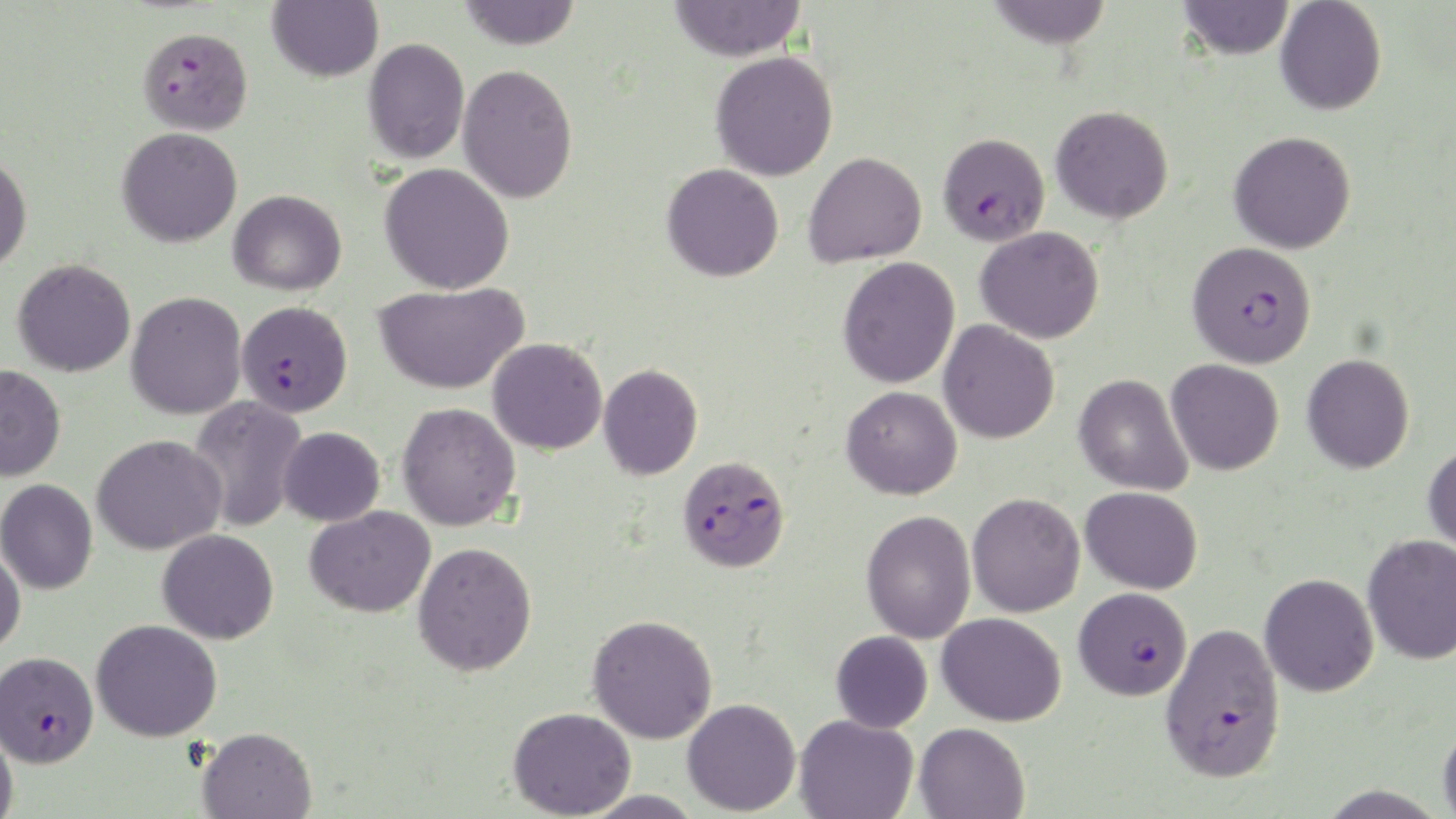
Summary:
  - Coordinate format: approximate bounding boxes as (x1,y1)-(x2,y2) corner pairs in pixels
  - Plasmodium falciparum-infected red blood cell locations: (137,26)-(253,135), (938,132)-(1050,246), (1187,241)-(1317,368), (236,301)-(353,416), (676,454)-(791,572), (1074,587)-(1192,700), (1160,623)-(1286,783), (0,650)-(98,767)
  - Uninfected red blood cell locations: (267,0)-(383,82), (456,0)-(581,50), (668,0)-(806,62), (986,0)-(1113,49), (1177,0)-(1294,60), (1275,0)-(1387,115), (363,37)-(470,164), (710,51)-(838,181), (457,64)-(578,204), (1051,105)-(1173,223), (116,126)-(243,248), (1228,131)-(1356,254), (0,152)-(32,273), (803,152)-(927,268), (380,163)-(515,294), (661,163)-(784,282), (228,189)-(346,295), (975,226)-(1104,344), (837,256)-(960,388), (12,258)-(136,377), (373,281)-(529,395), (126,291)-(247,420), (938,320)-(1060,444), (487,338)-(608,455), (1302,353)-(1414,474), (1166,359)-(1284,476), (599,363)-(703,480), (0,364)-(66,481), (1074,373)-(1193,496), (841,386)-(962,500), (188,396)-(308,532), (397,402)-(522,531), (279,426)-(385,526), (91,434)-(227,555), (1423,444)-(1456,556), (0,479)-(98,594), (1081,486)-(1203,594), (967,492)-(1086,617), (305,506)-(436,618), (861,510)-(976,643), (157,528)-(279,644), (1362,533)-(1456,664), (413,541)-(537,676), (0,545)-(26,655), (1259,573)-(1379,697), (937,612)-(1067,726), (587,614)-(718,744), (91,618)-(222,742), (831,630)-(933,733), (682,698)-(801,816), (508,706)-(636,818), (794,714)-(918,819), (914,722)-(1030,819), (1438,722)-(1456,819), (0,725)-(19,818), (197,726)-(317,818), (580,790)-(706,818)
  - Slide-level diagnosis: Plasmodium falciparum
  - Stain: May-Grünwald-Giemsa
  - Modality: light microscopy
  - Image size: 1456×819 pixels
  - Magnification: 1000x
  - Preparation: thin blood smear
  - Field of view: one of a larger specimen